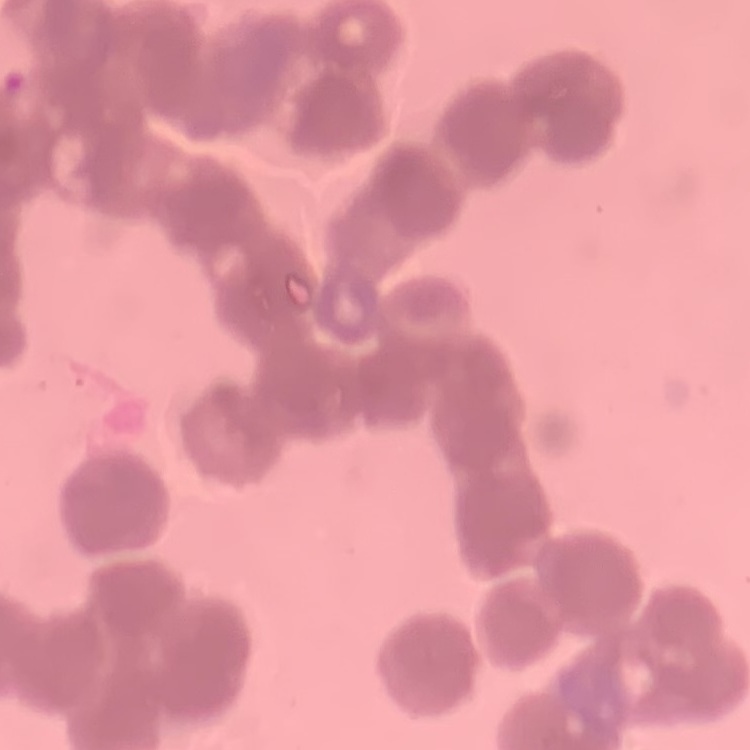
Summary:
  - Erythrocyte morphology: rouleaux formation
  - Stain: Field's or Giemsa
  - Preparation: thin blood film
  - Image type: one tile cut from a larger photomicrograph